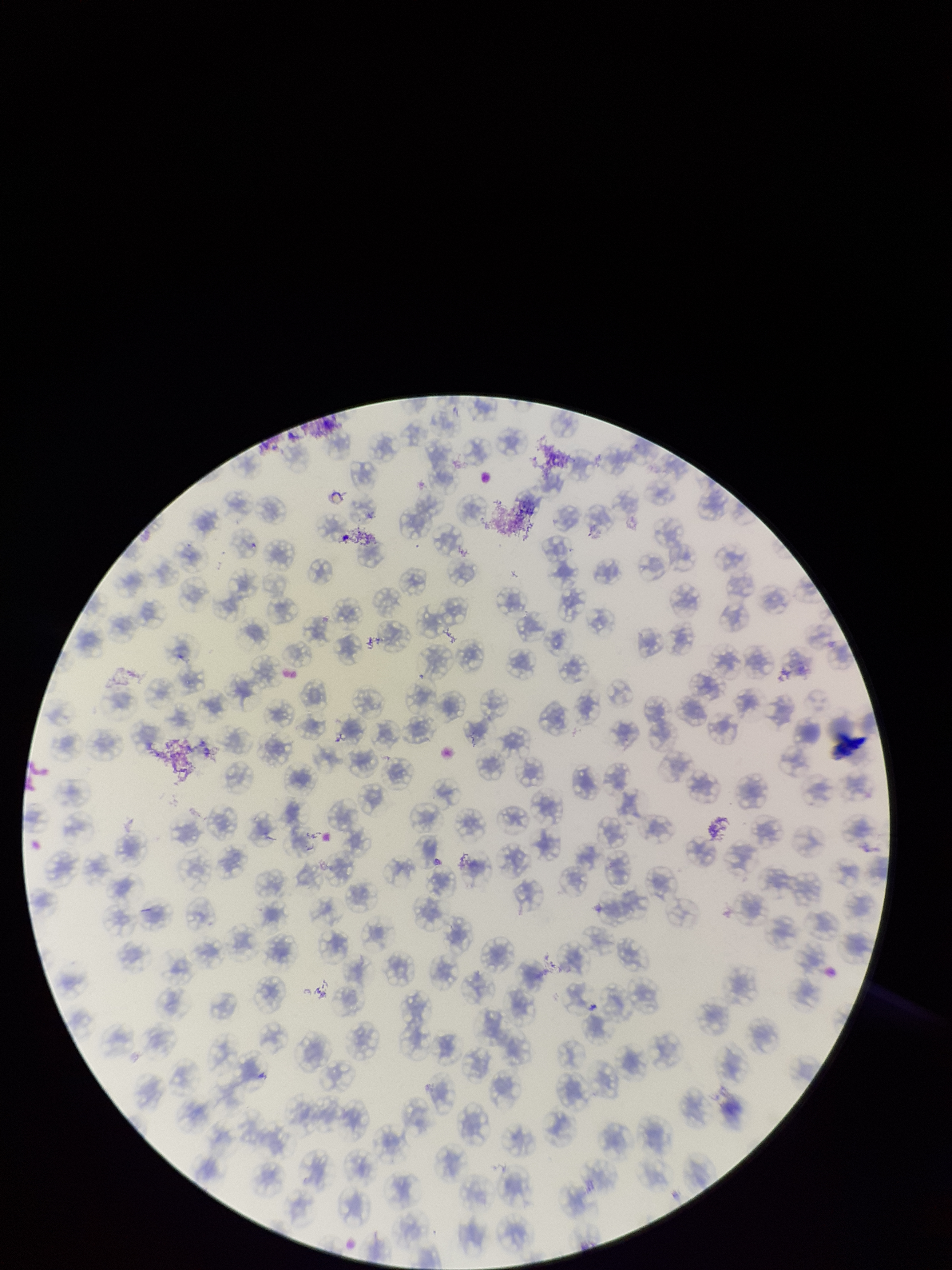

Red blood cell count: 130. Parasitized red blood cell count: 0. Preparation: thin smear. Stained with Giemsa. Patient malaria status: negative. Single field of view. Image is 952×1270 pixels. Parasitized red blood cells: none identified. Smartphone photograph taken through the eyepiece of a microscope.